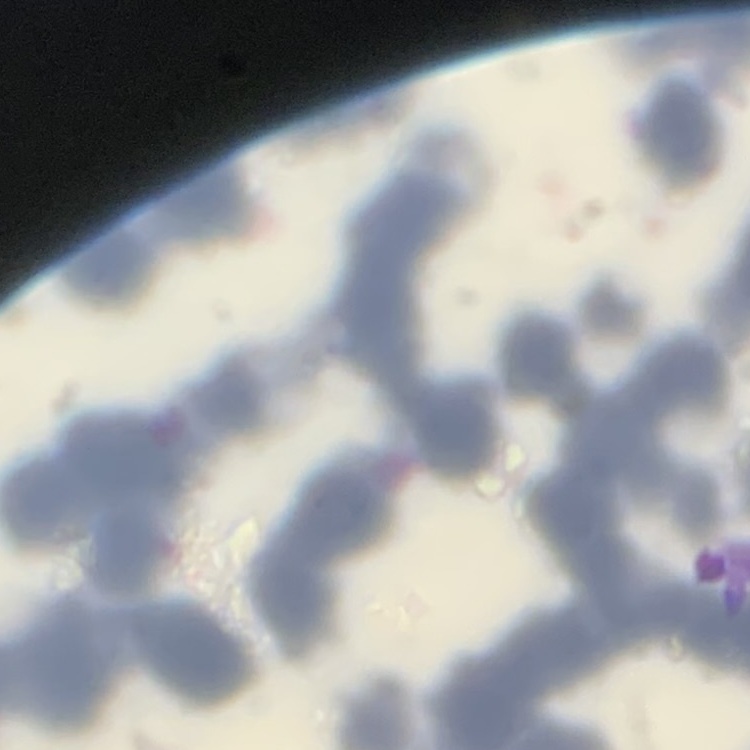
erythrocyte morphology = rouleaux formation
stain = Field's or Giemsa
image type = square crop of a larger photomicrograph
preparation = thin blood film